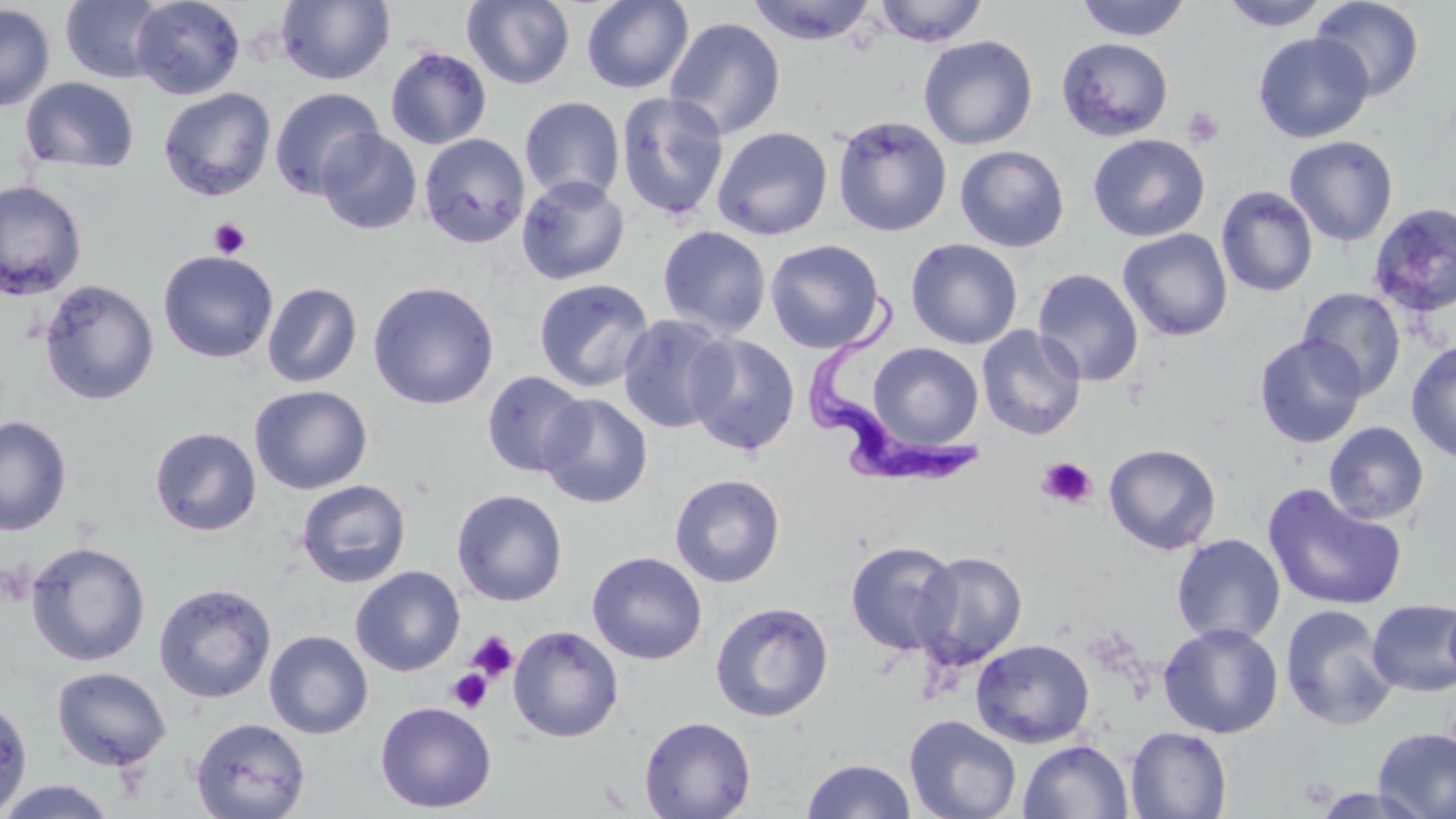

Approximate bounding boxes as (x1,y1)-(x2,y2) corner pairs in pixels. Uninfected red blood cell locations: (60,0)-(168,83), (131,0)-(245,99), (581,0)-(694,94), (873,0)-(988,47), (1075,0)-(1190,41), (1221,0)-(1329,31), (1310,0)-(1424,100), (276,1)-(395,85), (462,1)-(576,89), (747,1)-(879,45), (0,3)-(55,112), (664,16)-(786,140), (1253,32)-(1374,143), (918,35)-(1038,150), (1057,36)-(1174,141), (385,46)-(492,150), (20,77)-(139,174), (158,87)-(276,202), (269,87)-(385,199), (616,91)-(730,222), (519,96)-(625,203), (831,115)-(952,237), (712,126)-(833,241), (317,129)-(422,235), (419,134)-(530,248), (1087,134)-(1210,241), (1284,135)-(1399,246), (955,145)-(1069,252), (516,174)-(630,285), (0,179)-(87,300), (1216,186)-(1318,297), (1366,202)-(1456,319), (657,225)-(771,340), (1117,228)-(1234,342), (905,238)-(1023,349), (765,239)-(886,353), (158,250)-(278,363), (1032,268)-(1144,387), (533,278)-(654,393), (39,279)-(159,405), (367,280)-(500,410), (262,282)-(363,387), (1298,287)-(1406,399), (618,313)-(733,435), (976,325)-(1087,440), (684,333)-(801,455), (1254,333)-(1367,448), (1406,340)-(1456,464), (868,342)-(984,449), (481,370)-(589,477), (249,385)-(372,495), (539,393)-(653,508), (0,415)-(72,536), (1323,421)-(1429,525), (150,426)-(261,537), (1104,443)-(1221,554), (669,473)-(786,588), (295,479)-(412,588), (1262,483)-(1407,612), (451,489)-(568,607), (1171,533)-(1286,645), (25,540)-(151,667), (845,540)-(960,656), (912,550)-(1028,671), (587,551)-(707,665), (350,565)-(465,676), (153,582)-(276,703), (1367,599)-(1456,697), (710,601)-(834,722), (1279,604)-(1400,731), (1158,622)-(1284,739), (508,625)-(624,743), (264,630)-(373,740), (971,638)-(1095,748), (52,666)-(172,771), (0,696)-(32,816), (375,701)-(497,813), (904,715)-(1021,819), (191,716)-(310,819), (639,716)-(756,819), (1126,726)-(1233,818), (1373,726)-(1456,819), (1018,739)-(1134,819), (802,758)-(916,818), (0,778)-(118,818), (1306,787)-(1439,818). Platelet locations: (1182,106)-(1224,149), (209,217)-(250,259), (1036,456)-(1097,509), (466,632)-(518,683), (446,668)-(492,714). Trypanosoma brucei locations: (807,285)-(983,490). Slide-level diagnosis: Trypanosoma brucei. May-Grünwald-Giemsa stain. Light microscopy. Image is 1456×819 pixels. 1000x magnification. Single field of view. Thin blood smear.